Classify this cell by malaria status.
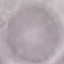
Uninfected.

Summary:
  - Capture: smartphone camera at the microscope eyepiece
  - Image type: automatically extracted cell patch, resized to 64 × 64 pixels
  - Preparation: thin smear
  - Stain: Giemsa